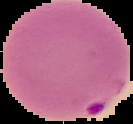

Summary:
  - Preparation: thin blood smear
  - Image type: segmented cell region on a black background
  - Image size: 133×124 pixels
  - Result: malaria parasites detected